Name the cell type shown.
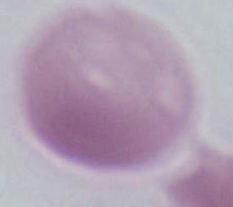
This is an erythrocyte.

Summary:
  - Magnification: 1000x
  - Modality: micrograph